Locate every blood parasite and identify its species.
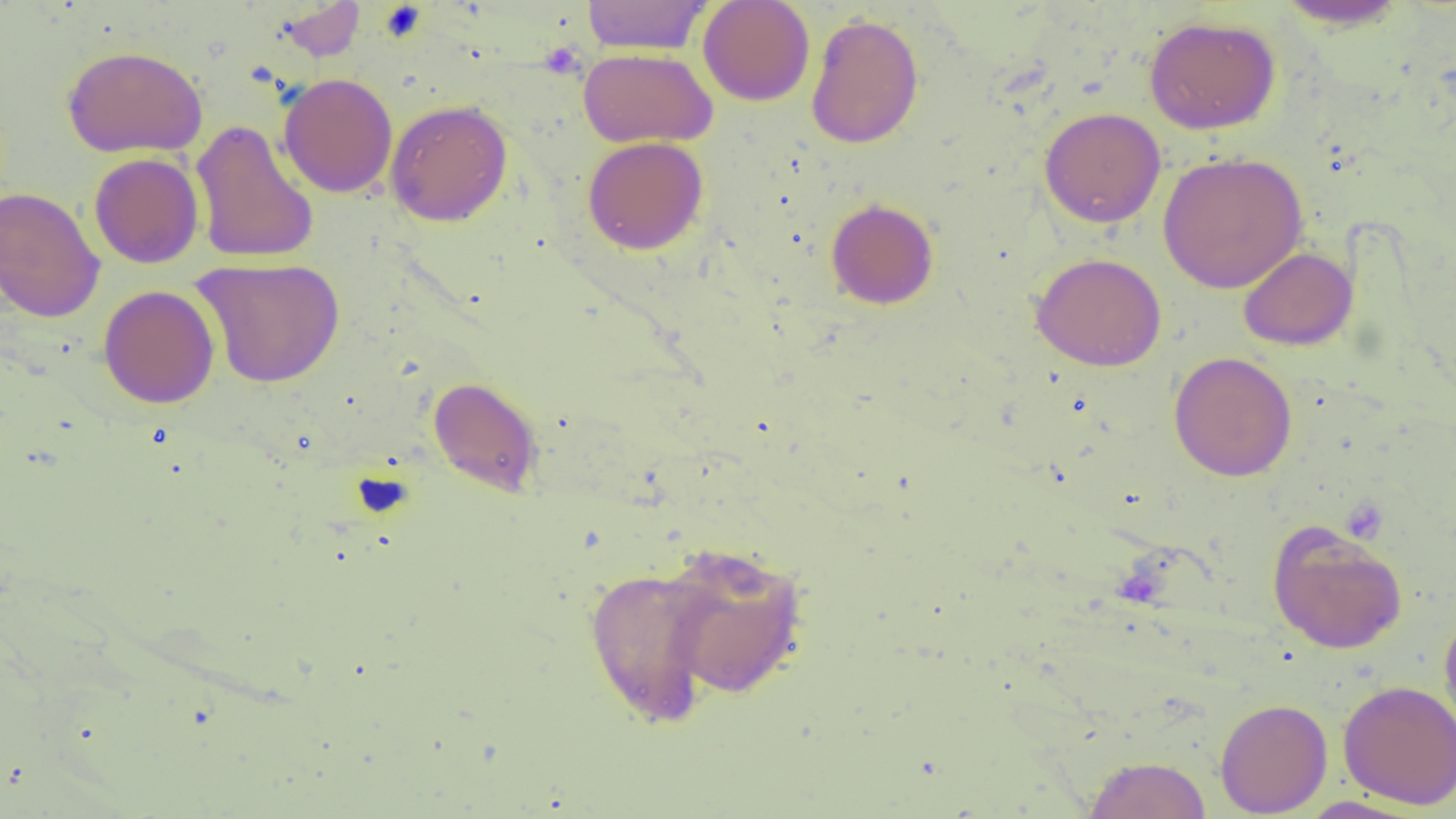
No blood parasites observed.

{
  "slide_level_diagnosis": "negative for blood parasites",
  "magnification": "1000x",
  "platelet_locations": "approximate bounding boxes as [x1, y1, x2, y2] in pixels: [378, 4, 428, 41], [538, 43, 585, 80]",
  "preparation": "thin blood smear",
  "field_of_view": "one of a larger specimen",
  "modality": "optical microscopy",
  "uninfected_red_blood_cell_locations": "approximate bounding boxes as [x1, y1, x2, y2] in pixels: [581, 0, 713, 55], [697, 0, 815, 106], [273, 1, 367, 62], [1273, 1, 1412, 30], [806, 12, 924, 149], [1144, 15, 1282, 134], [61, 45, 208, 157], [578, 48, 718, 148], [278, 72, 398, 198], [385, 99, 513, 227], [1039, 107, 1166, 228], [190, 118, 319, 264], [582, 136, 709, 254], [1158, 152, 1308, 293], [89, 153, 204, 269], [0, 187, 105, 323], [825, 198, 939, 310], [1238, 247, 1357, 351], [1031, 252, 1167, 371], [192, 257, 345, 388], [98, 284, 220, 409], [1169, 351, 1297, 481], [428, 377, 543, 497], [1267, 520, 1408, 655], [656, 542, 811, 700], [584, 565, 722, 728], [1438, 608, 1456, 741], [1338, 680, 1456, 809], [1215, 698, 1332, 817], [1083, 755, 1212, 818], [1293, 796, 1429, 818]",
  "image_size": "1456×819 pixels"
}